State which parasite is depicted.
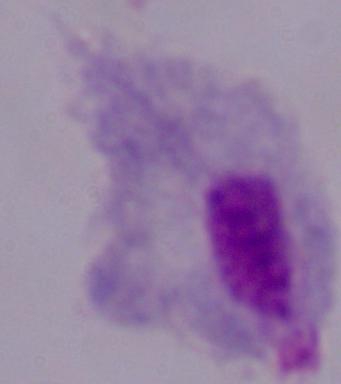

A trichomonad.

1000x magnification. Photomicrograph.